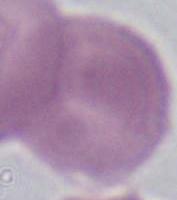
1000x magnification. An erythrocyte is seen. Micrograph.